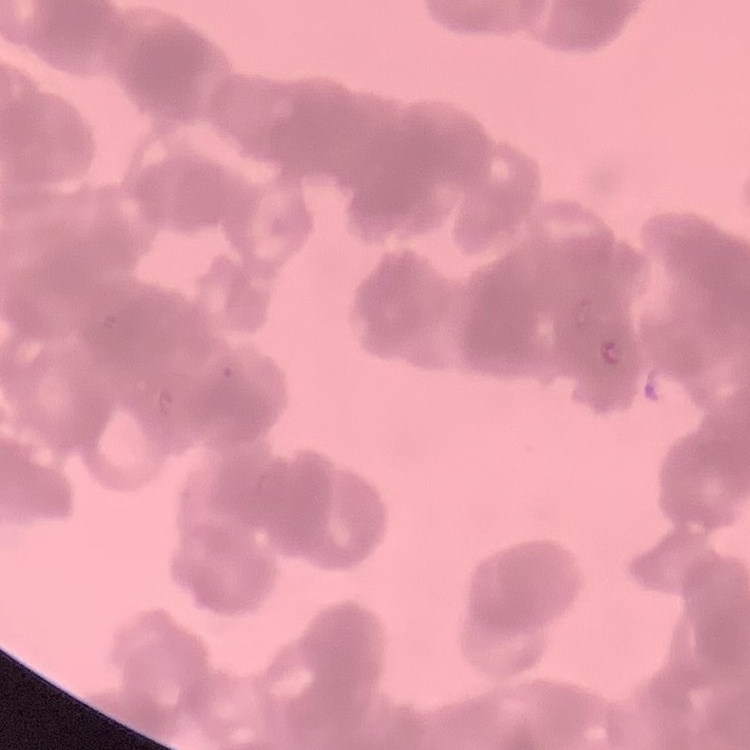
erythrocyte morphology = rouleaux formation
image type = square crop of a larger photomicrograph
stain = Field's or Giemsa
preparation = thin blood smear